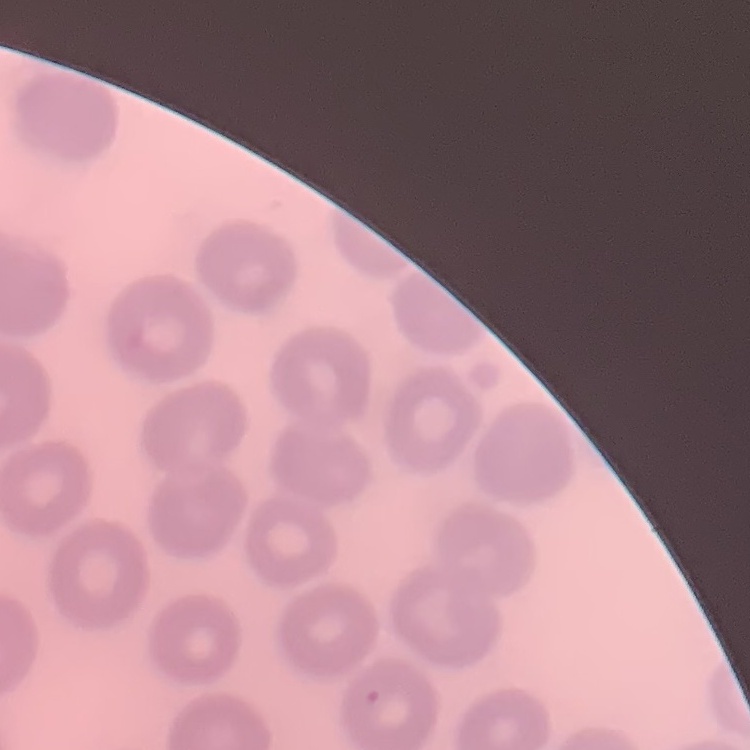
Summary:
  - Erythrocyte morphology: no rouleaux formation
  - Preparation: thin peripheral smear
  - Stain: Field's or Giemsa
  - Image type: one tile cut from a larger photomicrograph